Assess this cell for malaria.
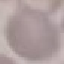

Uninfected.

Acquired by smartphone through the microscope eyepiece. Giemsa-stained preparation. Thin smear of blood. Cell patch, automatically extracted from a larger field of view and resized to 64 × 64 pixels.